Comment on the morphology of the red blood cells.
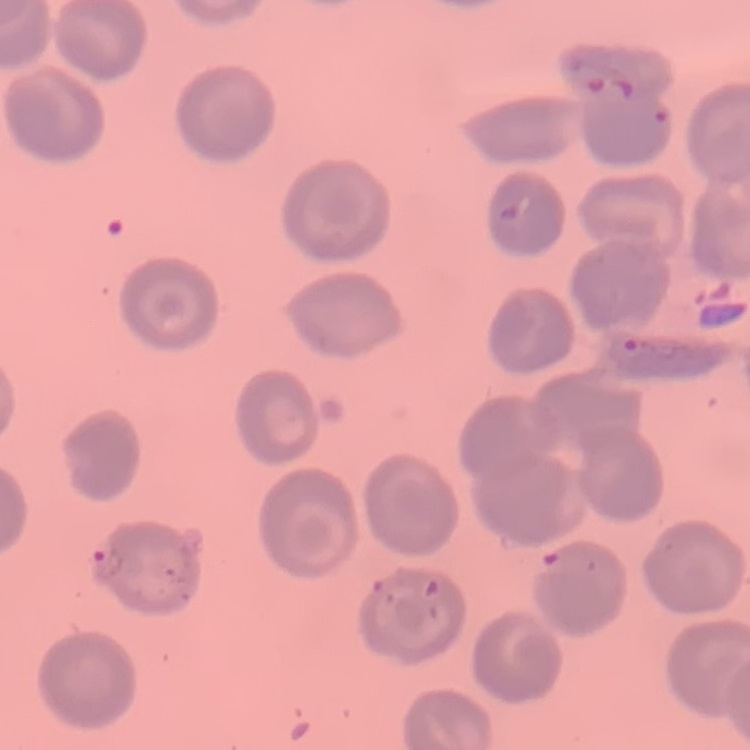
No rouleaux formation.

Square crop of a larger photomicrograph. Thin blood smear. Field's or Giemsa stain.